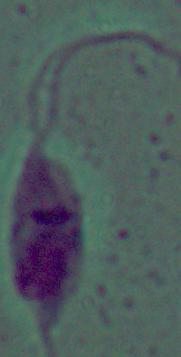
Summary:
  - Identification: Leishmania
  - Modality: photomicrograph
  - Magnification: 1000x